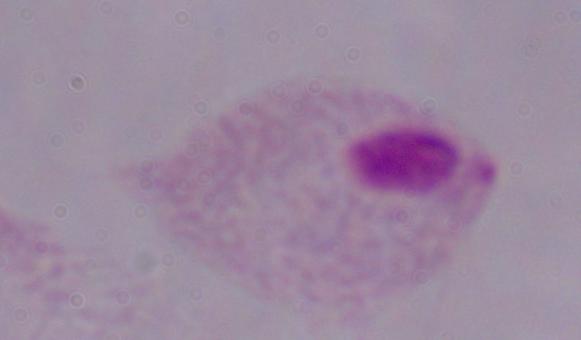 Micrograph. Captured at 1000x magnification. A trichomonad is seen.